Give the preparation type.
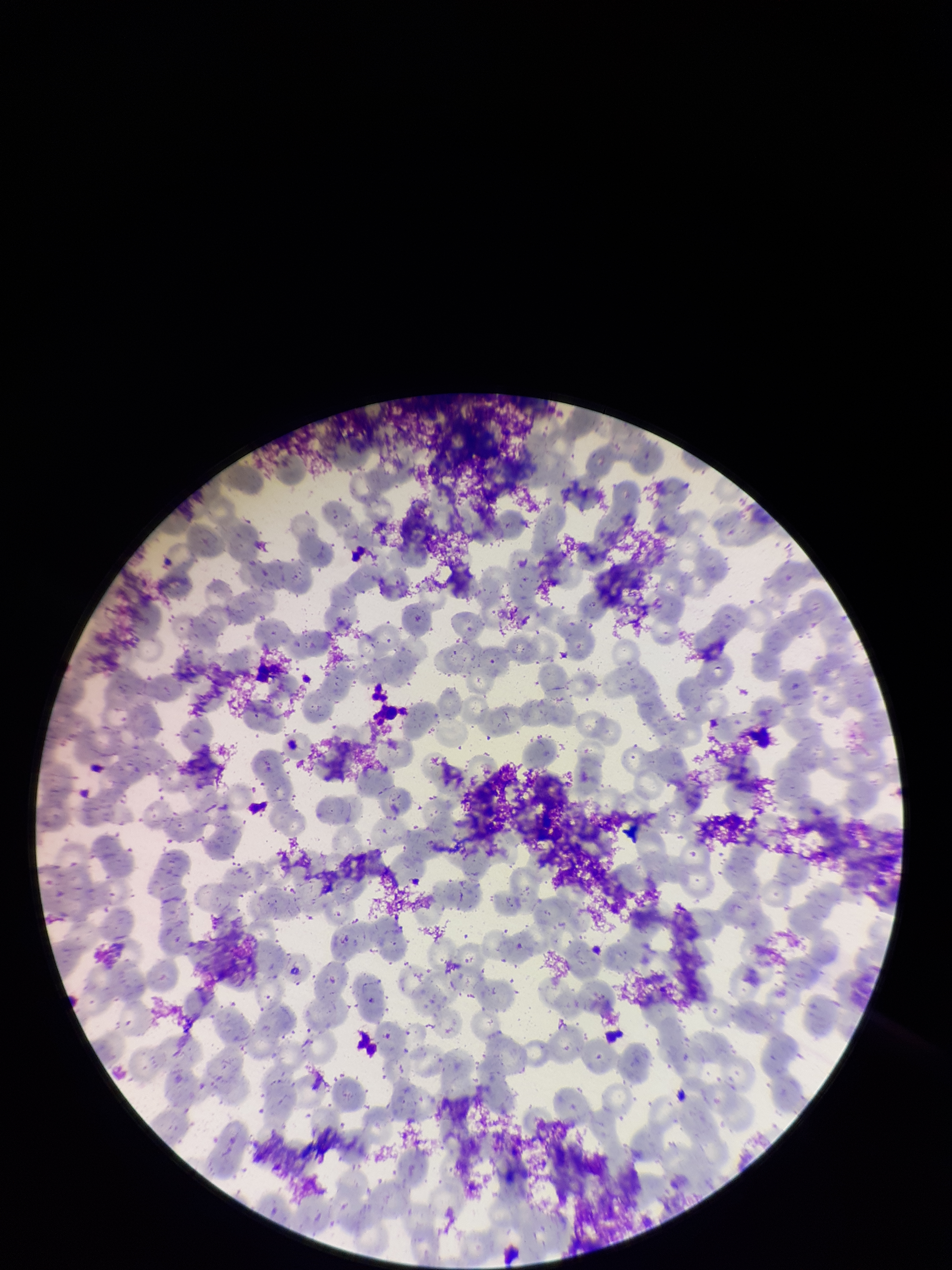

It is a thin blood smear.

Smartphone photograph taken through the eyepiece of a microscope. Parasitized red blood cell count: 0. Image is 952×1270 pixels. Parasitized red blood cells: none identified. One field from this slide. Red blood cell count: 288. Patient malaria status: negative. Giemsa stain.